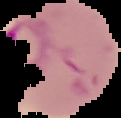
Image is 121×118 pixels. Malaria status: parasitized. From a thin blood smear. The area outside the segmented cell region is set to black.